Assess the morphology of the erythrocytes.
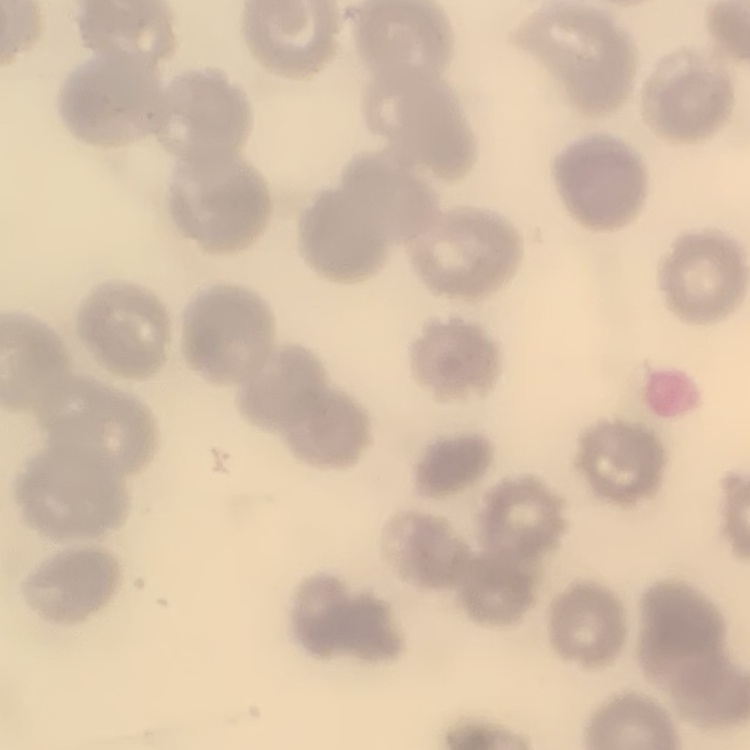

No rouleaux formation.

Thin blood film. Field's or Giemsa stain. Square crop of a larger photomicrograph.